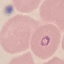
Summary:
  - Result: malaria parasites identified
  - Stain: Giemsa
  - Capture: smartphone camera at the microscope eyepiece
  - Image type: cell patch, automatically extracted from a larger field of view and resized to 64 × 64 pixels
  - Preparation: thin blood film